Identify the preparation type.
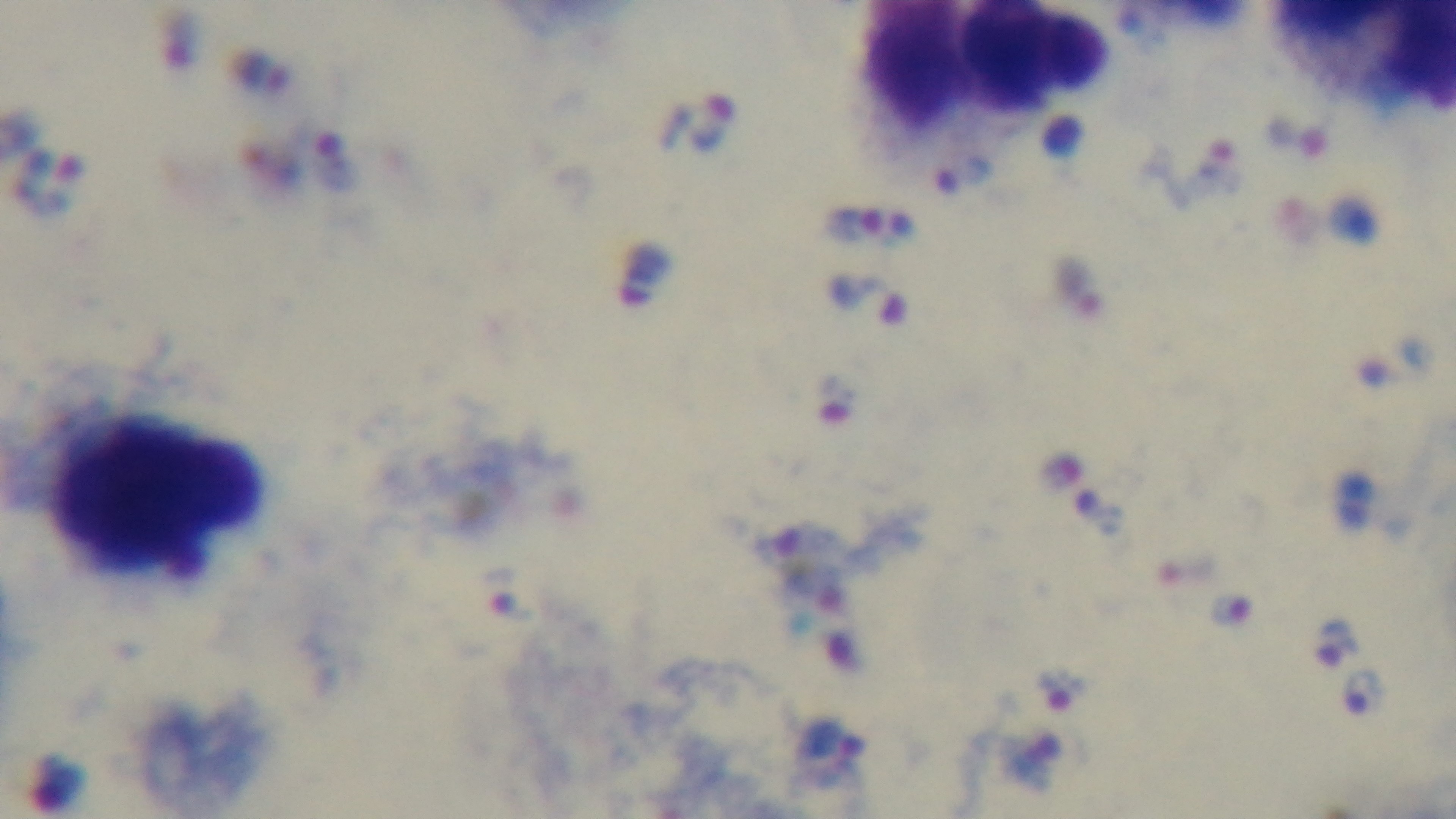
A thick smear.

Summary:
  - Field of view: one from the slide
  - Modality: light microscopy
  - Stain: Giemsa
  - Objective: 100x oil immersion
  - Malaria status: positive
  - Capture: mounted 4K digital camera